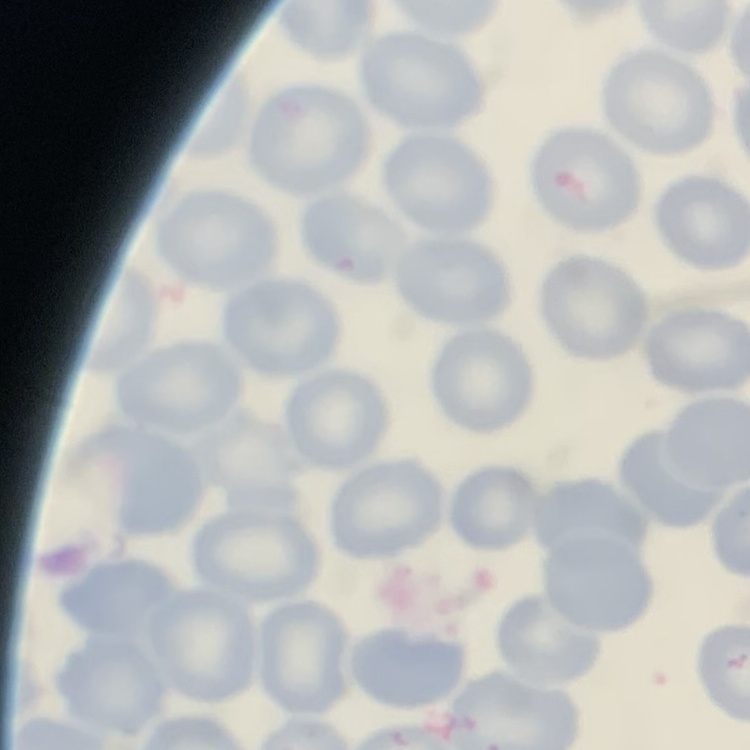

The erythrocytes exhibit no rouleaux formation. One tile cut from a larger photomicrograph. Stained with either Field's or Giemsa. Thin peripheral smear.